Outline each blood parasite and name the species.
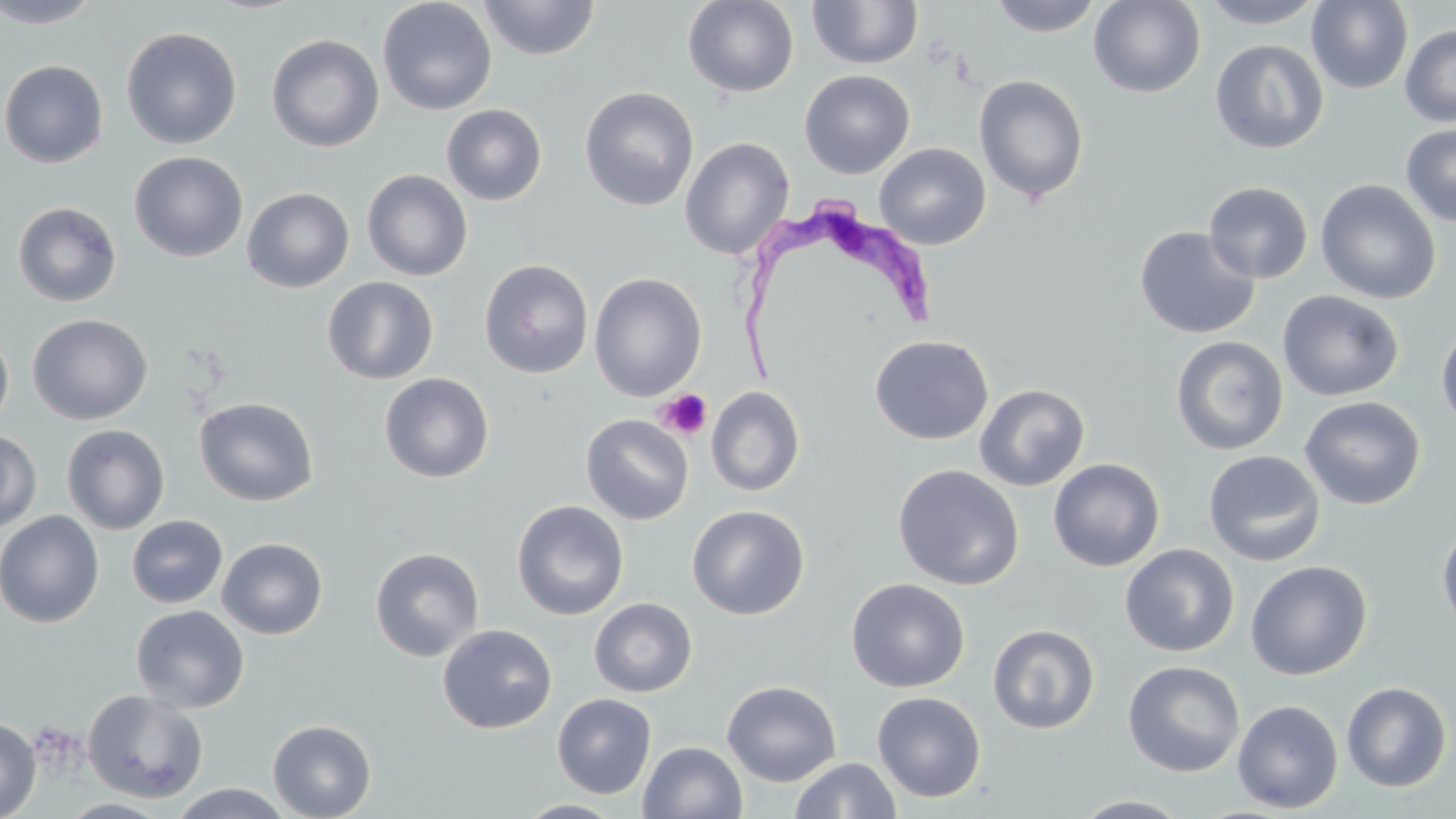

Approximate bounding boxes as (x1,y1)-(x2,y2) corner pairs in pixels.
Trypanosoma brucei: (733,196)-(932,383).
No Plasmodium falciparum, Plasmodium ovale, Plasmodium malariae, Plasmodium vivax, or Babesia divergens observed.

{
  "slide_level_diagnosis": "Trypanosoma brucei",
  "stain": "May-Grünwald-Giemsa",
  "field_of_view": "one of a larger specimen",
  "modality": "light microscopy",
  "magnification": "1000x",
  "platelet_locations": "approximate bounding boxes as (x1,y1)-(x2,y2) corner pairs in pixels: (655,389)-(711,441)",
  "uninfected_red_blood_cell_locations": "approximate bounding boxes as (x1,y1)-(x2,y2) corner pairs in pixels: (1,0)-(105,28), (377,0)-(498,116), (479,0)-(600,60), (683,0)-(799,98), (988,0)-(1104,37), (1088,0)-(1206,98), (1198,0)-(1327,28), (807,1)-(923,70), (1306,1)-(1413,94), (1400,24)-(1456,126), (120,27)-(242,149), (267,34)-(384,152), (1209,39)-(1329,154), (0,60)-(108,168), (799,70)-(915,179), (973,74)-(1090,205), (579,86)-(699,211), (441,103)-(547,206), (1400,123)-(1456,227), (680,136)-(795,261), (874,143)-(991,249), (128,151)-(248,262), (362,169)-(472,281), (1315,179)-(1441,304), (1204,181)-(1313,284), (242,187)-(354,293), (12,201)-(122,307), (1134,225)-(1260,339), (479,258)-(594,379), (589,273)-(707,401), (321,276)-(439,385), (1277,289)-(1404,401), (27,313)-(152,425), (1436,323)-(1456,433), (0,327)-(14,431), (870,335)-(994,445), (1171,335)-(1288,455), (379,372)-(495,483), (974,383)-(1090,491), (706,386)-(805,497), (1299,395)-(1425,510), (194,396)-(318,506), (580,414)-(693,525), (61,424)-(170,534), (0,429)-(41,533), (1203,450)-(1326,566), (1048,458)-(1165,571), (892,464)-(1024,590), (512,500)-(628,620), (687,504)-(810,620), (0,509)-(105,628), (126,515)-(228,609), (1437,521)-(1456,634), (216,537)-(328,639), (1119,543)-(1240,656), (370,547)-(484,662), (1245,560)-(1372,680), (846,577)-(969,693), (589,597)-(697,697), (130,605)-(249,713), (988,623)-(1100,734), (437,624)-(557,734), (1123,660)-(1245,777), (721,680)-(842,786), (1341,682)-(1452,792), (82,689)-(209,804), (872,691)-(986,802), (552,693)-(657,799), (1232,699)-(1343,813), (0,717)-(41,819), (267,719)-(376,819), (638,741)-(747,819), (790,757)-(900,818), (167,783)-(295,818), (1071,795)-(1194,818), (59,797)-(173,818), (514,800)-(628,818)",
  "preparation": "thin blood smear",
  "image_size": "1456×819 pixels"
}